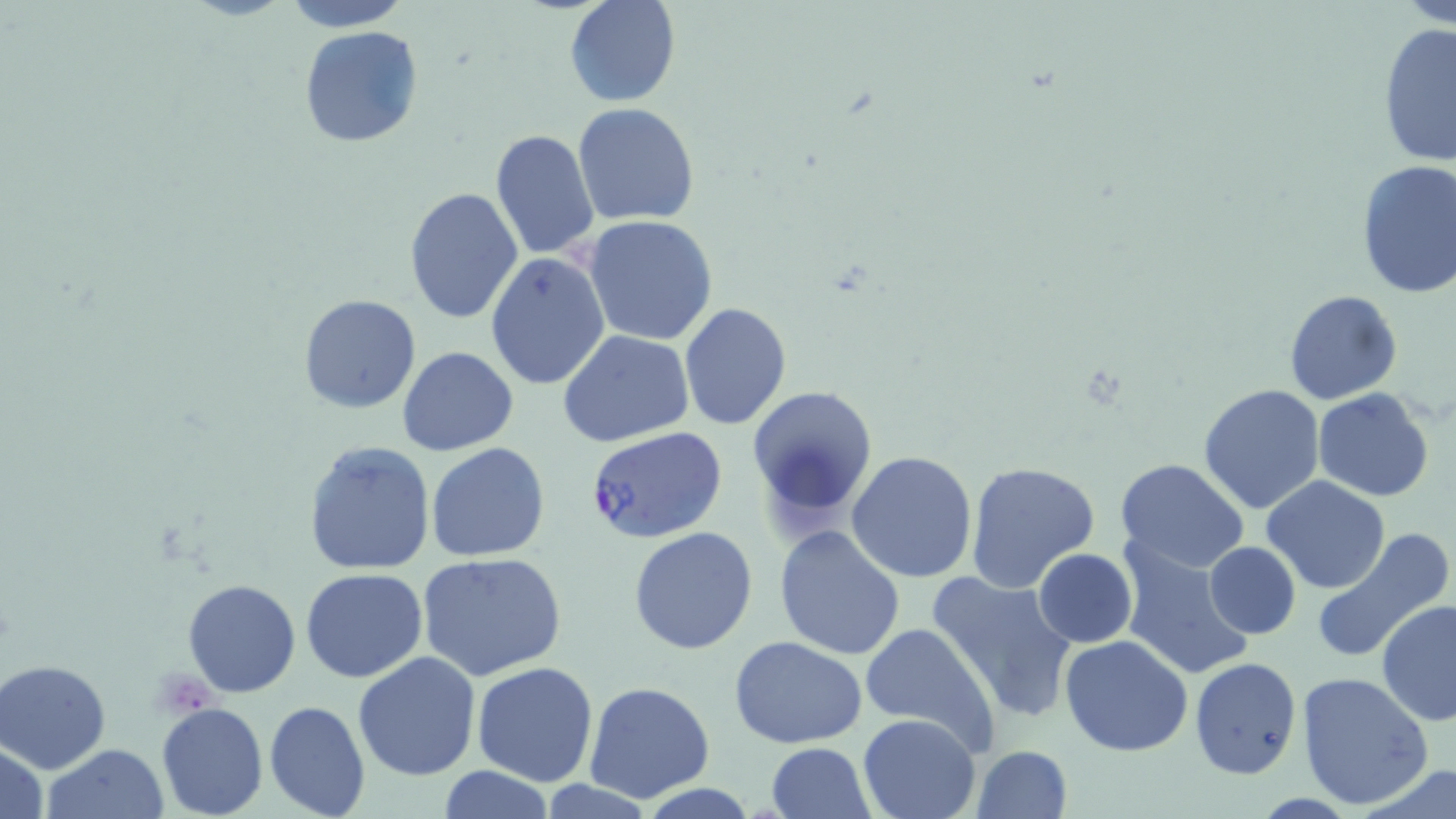
Approximate bounding boxes as [x1, y1, x2, y2] in pixels. Plasmodium falciparum-infected red blood cell locations: [585, 425, 728, 545]. Uninfected red blood cell locations: [280, 0, 415, 30], [564, 0, 680, 109], [1394, 0, 1456, 26], [1375, 21, 1456, 167], [298, 26, 423, 149], [572, 102, 701, 226], [489, 130, 600, 260], [1354, 159, 1456, 300], [403, 187, 524, 325], [584, 215, 718, 345], [485, 250, 611, 391], [1282, 290, 1402, 406], [297, 294, 422, 413], [679, 303, 791, 430], [559, 331, 696, 445], [397, 346, 519, 457], [745, 383, 877, 527], [1198, 384, 1326, 516], [1312, 389, 1434, 501], [303, 441, 435, 574], [425, 443, 551, 562], [846, 450, 978, 583], [1115, 458, 1251, 574], [966, 461, 1100, 595], [1263, 475, 1390, 594], [627, 526, 758, 655], [773, 526, 906, 660], [1310, 528, 1454, 663], [1117, 537, 1258, 682], [1203, 542, 1301, 638], [1032, 548, 1138, 647], [419, 553, 565, 681], [299, 568, 428, 683], [926, 569, 1078, 724], [181, 578, 302, 698], [1377, 599, 1456, 728], [859, 622, 996, 751], [1060, 635, 1193, 757], [730, 637, 869, 749], [353, 652, 481, 781], [1189, 656, 1303, 780], [0, 658, 112, 773], [472, 662, 599, 786], [1296, 671, 1433, 807], [584, 681, 715, 803], [264, 700, 370, 819], [156, 701, 269, 819], [858, 711, 981, 818], [1, 739, 48, 819], [767, 742, 875, 819], [40, 743, 172, 819], [970, 745, 1073, 819], [1361, 762, 1454, 819], [436, 765, 551, 819]. Slide-level diagnosis: Plasmodium falciparum. May-Grünwald-Giemsa-stained preparation. Single field of view. 1000x magnification. Thin blood film. Optical microscopy. Image is 1456×819 pixels.